Classify this cell by malaria status.
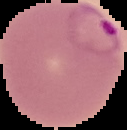
It is parasitized.

Summary:
  - Preparation: thin blood film
  - Image type: segmented cell region on a black background
  - Image size: 127×130 pixels